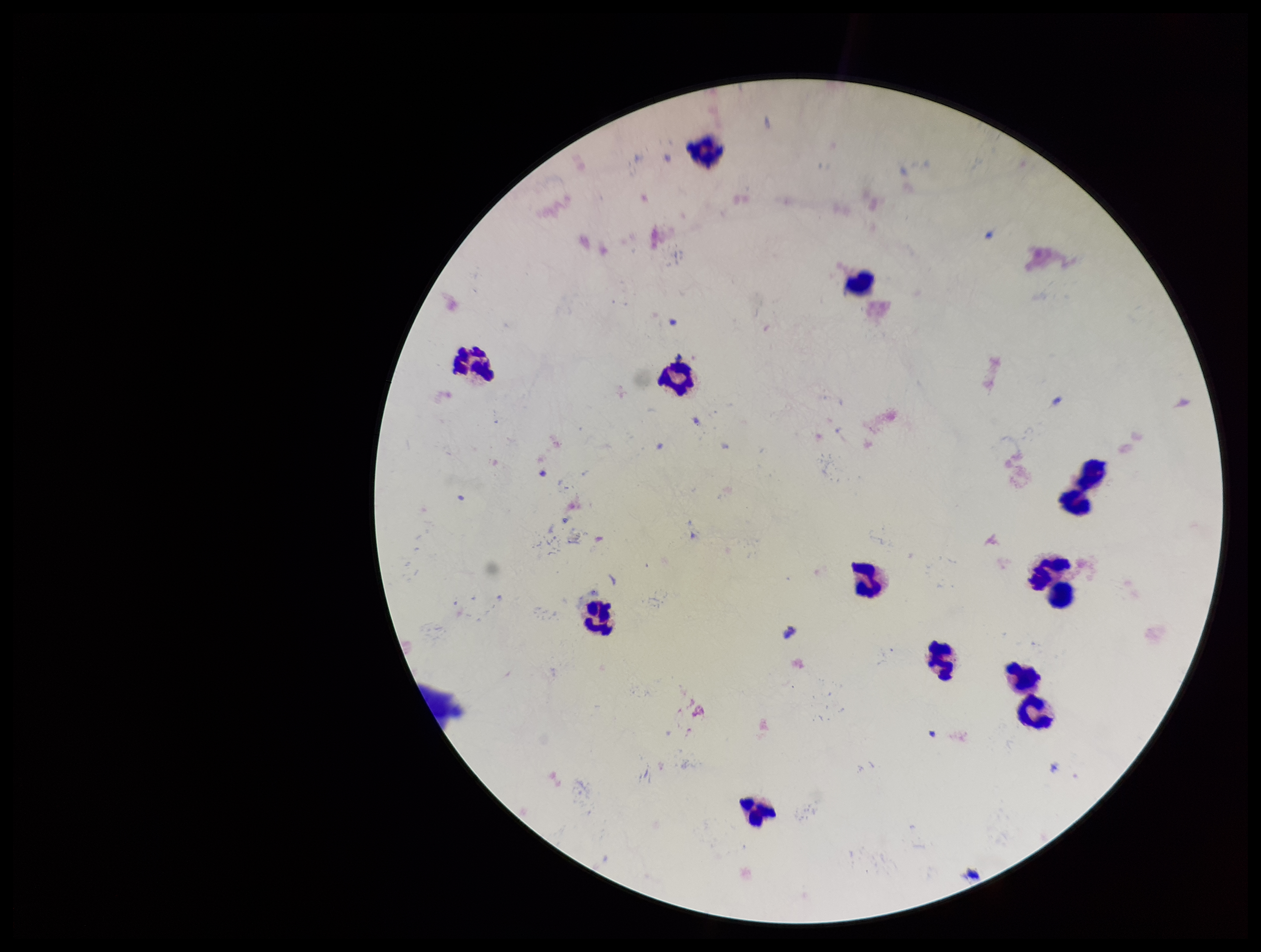

Summary:
  - Preparation: thick
  - Field of view: one from this slide
  - Plasmodium parasites: none identified
  - Parasite count: 0
  - Image size: 1261×952 pixels
  - Capture: smartphone photograph through the microscope eyepiece
  - Patient malaria status: negative
  - Leukocyte count: 13
  - Stain: Giemsa